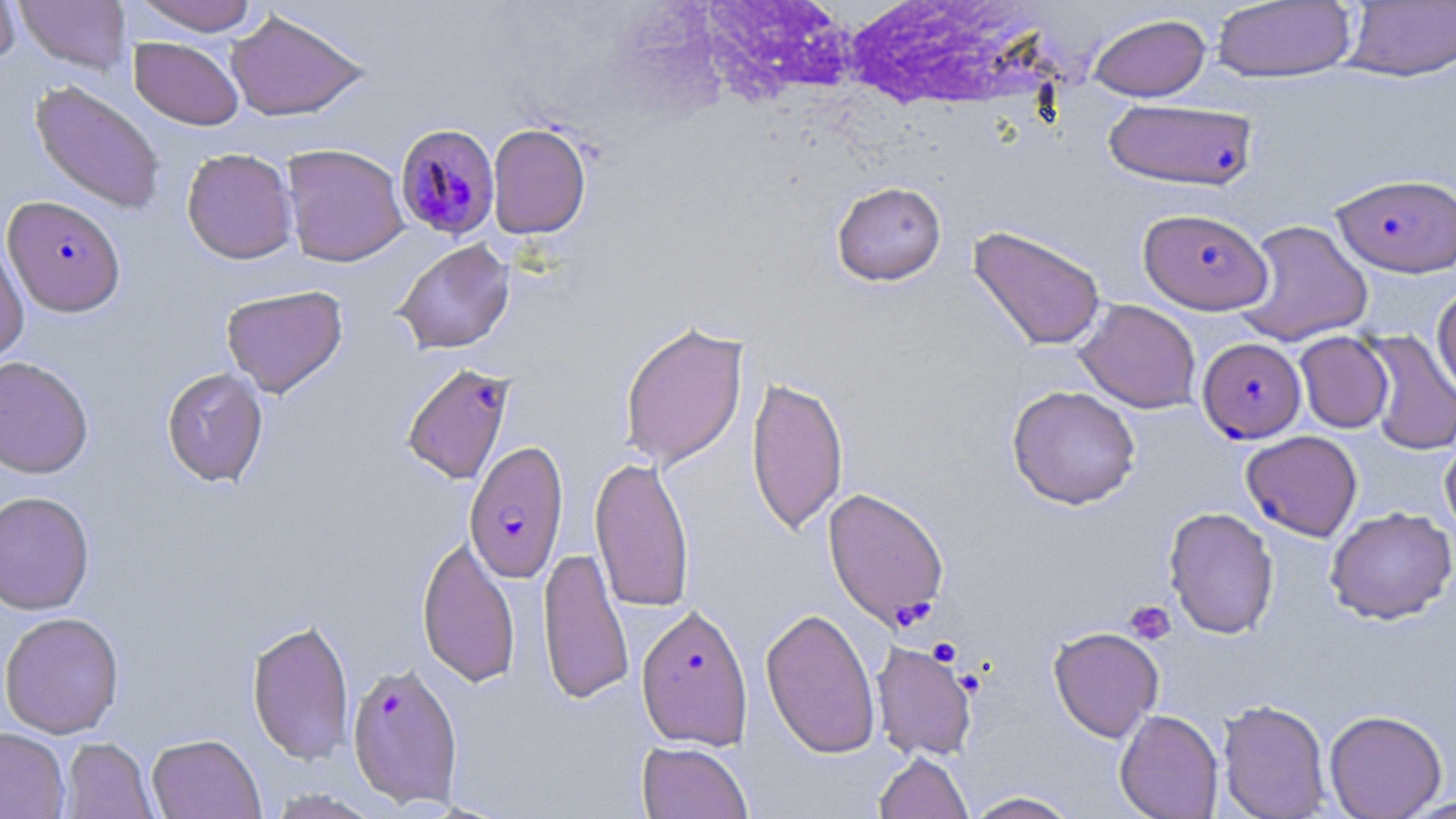
{
  "slide_level_diagnosis": "Plasmodium falciparum",
  "platelet_locations": "approximate bounding boxes as named x1/y1/x2/y2 corners in pixels: (x1=1124, y1=599, x2=1175, y2=645), (x1=928, y1=637, x2=962, y2=666)",
  "modality": "optical microscopy",
  "image_size": "1456×819 pixels",
  "magnification": "1000x",
  "field_of_view": "single",
  "preparation": "thin blood smear",
  "plasmodium_falciparum_infected_red_blood_cell_locations": "approximate bounding boxes as named x1/y1/x2/y2 corners in pixels: (x1=1096, y1=99, x2=1250, y2=191), (x1=396, y1=122, x2=500, y2=242), (x1=1331, y1=172, x2=1456, y2=278), (x1=2, y1=195, x2=125, y2=317), (x1=1139, y1=207, x2=1272, y2=314), (x1=1197, y1=337, x2=1306, y2=443), (x1=401, y1=362, x2=516, y2=485), (x1=1241, y1=430, x2=1363, y2=541), (x1=463, y1=440, x2=569, y2=583), (x1=822, y1=487, x2=950, y2=629), (x1=636, y1=603, x2=753, y2=750), (x1=346, y1=660, x2=464, y2=808)",
  "uninfected_red_blood_cell_locations": "approximate bounding boxes as named x1/y1/x2/y2 corners in pixels: (x1=0, y1=0, x2=21, y2=69), (x1=132, y1=0, x2=261, y2=35), (x1=14, y1=1, x2=131, y2=74), (x1=1212, y1=1, x2=1357, y2=83), (x1=1342, y1=1, x2=1456, y2=82), (x1=225, y1=9, x2=369, y2=121), (x1=1088, y1=13, x2=1211, y2=102), (x1=129, y1=37, x2=244, y2=130), (x1=29, y1=80, x2=166, y2=214), (x1=487, y1=123, x2=592, y2=240), (x1=281, y1=144, x2=409, y2=267), (x1=181, y1=147, x2=298, y2=264), (x1=831, y1=181, x2=946, y2=286), (x1=1234, y1=219, x2=1374, y2=346), (x1=968, y1=224, x2=1107, y2=351), (x1=0, y1=239, x2=29, y2=367), (x1=393, y1=239, x2=515, y2=354), (x1=221, y1=285, x2=348, y2=398), (x1=1431, y1=285, x2=1456, y2=401), (x1=1075, y1=299, x2=1201, y2=413), (x1=619, y1=321, x2=749, y2=469), (x1=1294, y1=331, x2=1394, y2=433), (x1=1361, y1=331, x2=1456, y2=456), (x1=0, y1=356, x2=94, y2=479), (x1=161, y1=367, x2=269, y2=488), (x1=745, y1=375, x2=849, y2=535), (x1=1007, y1=385, x2=1141, y2=509), (x1=1440, y1=436, x2=1456, y2=542), (x1=589, y1=455, x2=695, y2=613), (x1=0, y1=490, x2=95, y2=615), (x1=1164, y1=506, x2=1279, y2=640), (x1=1325, y1=506, x2=1456, y2=624), (x1=416, y1=532, x2=521, y2=688), (x1=538, y1=545, x2=634, y2=705), (x1=760, y1=606, x2=881, y2=759), (x1=0, y1=611, x2=125, y2=739), (x1=246, y1=618, x2=355, y2=766), (x1=1048, y1=626, x2=1164, y2=742), (x1=871, y1=640, x2=977, y2=762), (x1=1217, y1=698, x2=1331, y2=819), (x1=1114, y1=709, x2=1224, y2=819), (x1=1324, y1=709, x2=1447, y2=819), (x1=0, y1=727, x2=69, y2=819), (x1=147, y1=733, x2=265, y2=819), (x1=60, y1=738, x2=157, y2=819), (x1=636, y1=740, x2=753, y2=819), (x1=873, y1=751, x2=973, y2=819), (x1=265, y1=788, x2=384, y2=818), (x1=964, y1=790, x2=1082, y2=818)",
  "stain": "May-Grünwald-Giemsa"
}